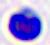
Photomicrograph. A leukocyte is shown. Captured at 400x magnification.